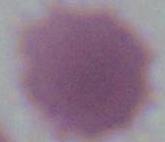

Summary:
  - Identification: erythrocyte
  - Magnification: 1000x
  - Modality: micrograph